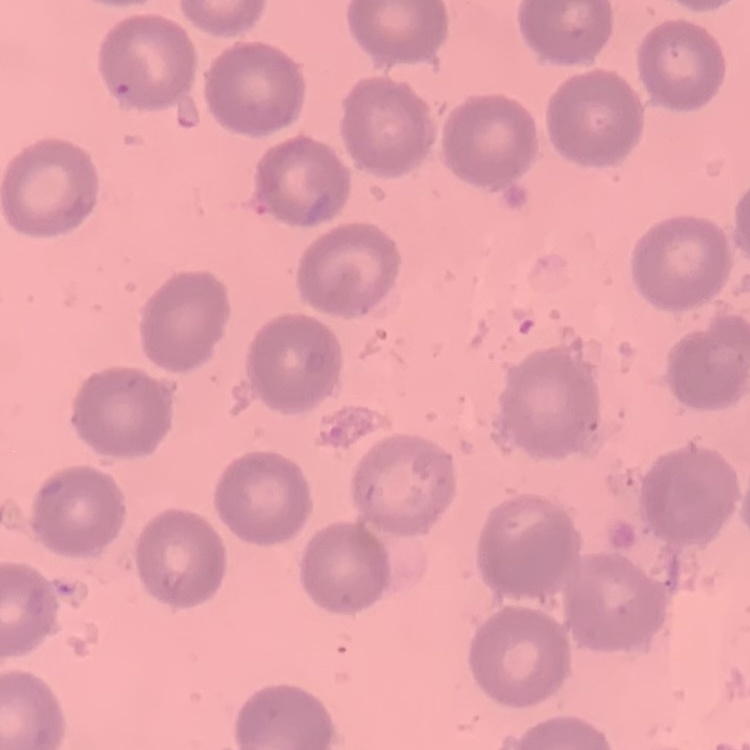

erythrocyte morphology = no rouleaux formation
image type = square crop of a larger photomicrograph
preparation = thin blood film
stain = Field's or Giemsa